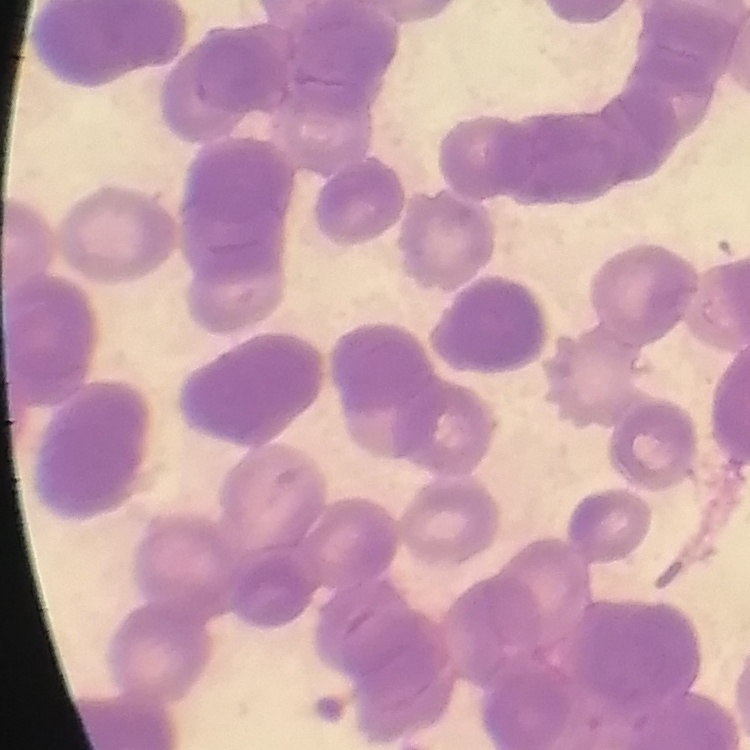
Summary:
  - Red blood cell morphology: rouleaux formation
  - Image type: square crop of a larger photomicrograph
  - Preparation: thin peripheral smear
  - Stain: Field's or Giemsa